Give the position of every leukocyte visible.
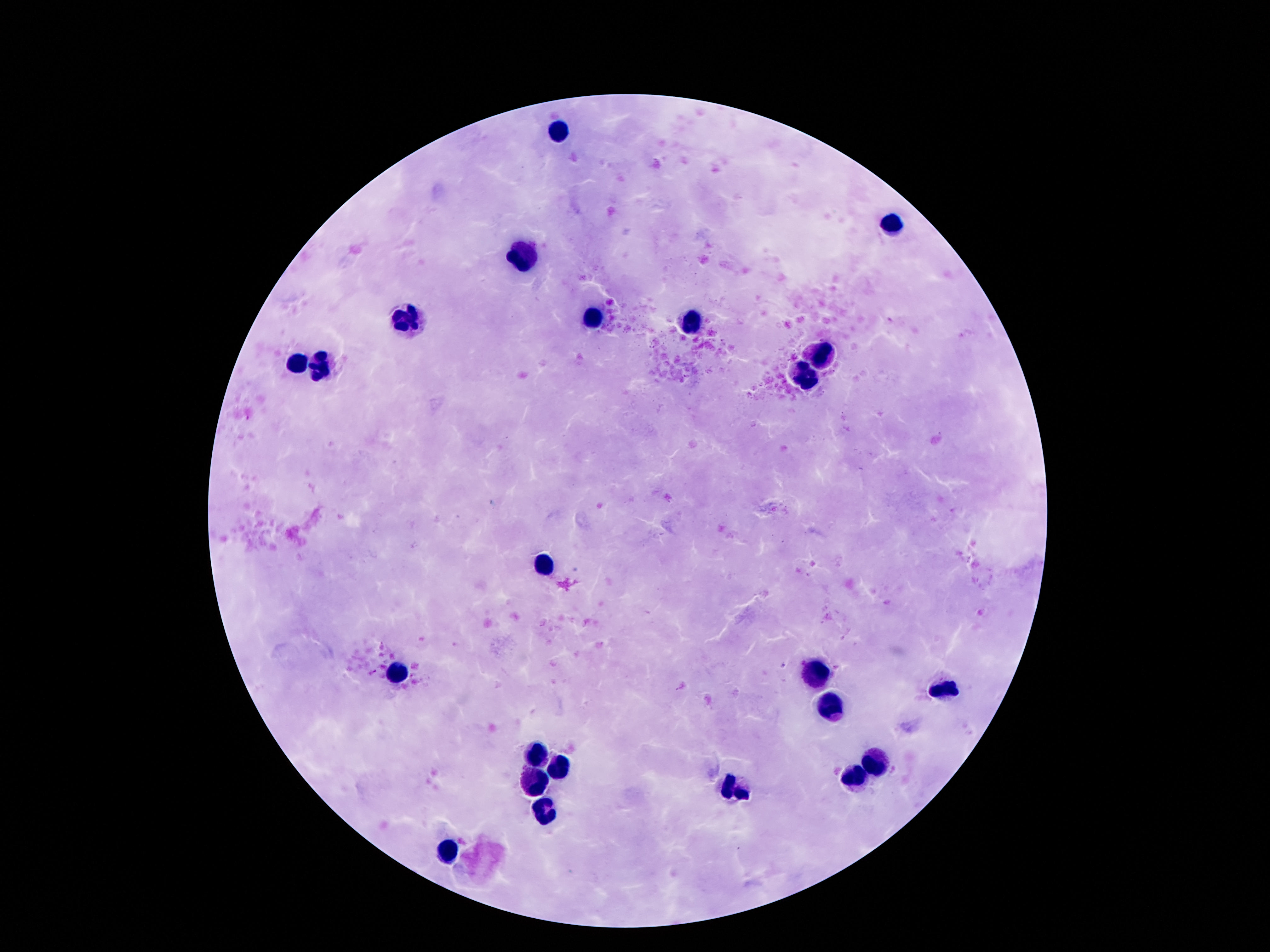
Approximate object centers, in pixels from the top-left corner.
Leukocytes: (x=557, y=130), (x=894, y=223), (x=521, y=258), (x=409, y=319), (x=590, y=322), (x=693, y=322), (x=822, y=355), (x=292, y=363), (x=320, y=369), (x=805, y=378), (x=544, y=561), (x=816, y=670), (x=394, y=672), (x=943, y=689), (x=829, y=711), (x=534, y=754), (x=876, y=760), (x=562, y=767), (x=540, y=782), (x=850, y=782), (x=734, y=790), (x=544, y=812), (x=452, y=853).

100x magnification. Photographed through the microscope eyepiece with a smartphone camera. Patient malaria status: uninfected. Giemsa stain. Single field of view. Image is 1270×952 pixels. Thick peripheral-blood smear.